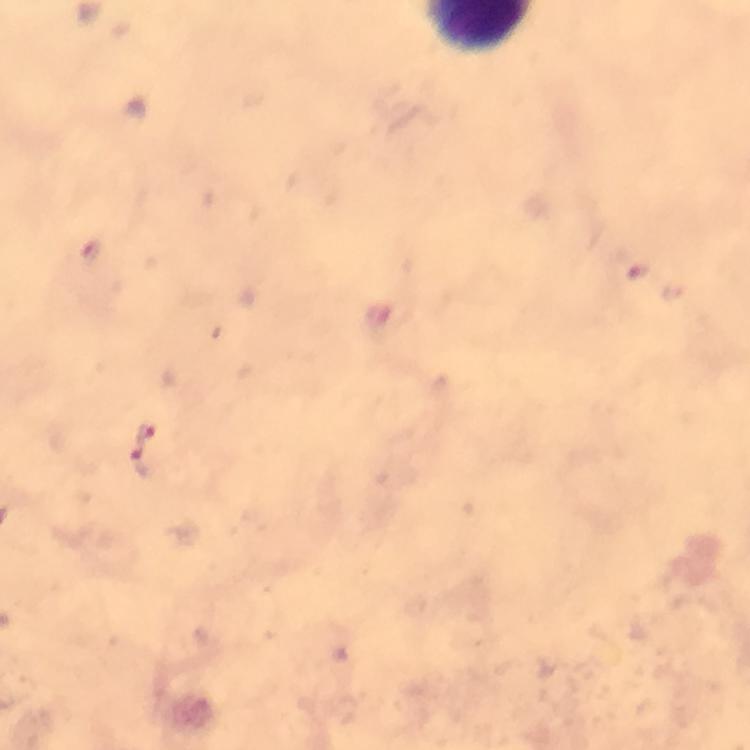

magnification = 100x
context = from a diagnostic examination for malaria
preparation = thick blood smear
cropped from = a single field of view
image size = 750×750 pixels
stain = Giemsa
capture = smartphone camera through the microscope
malaria parasite locations = approximate object centers, in pixels from the top-left corner: (x=637, y=270), (x=146, y=434), (x=144, y=465)
immersion oil = used